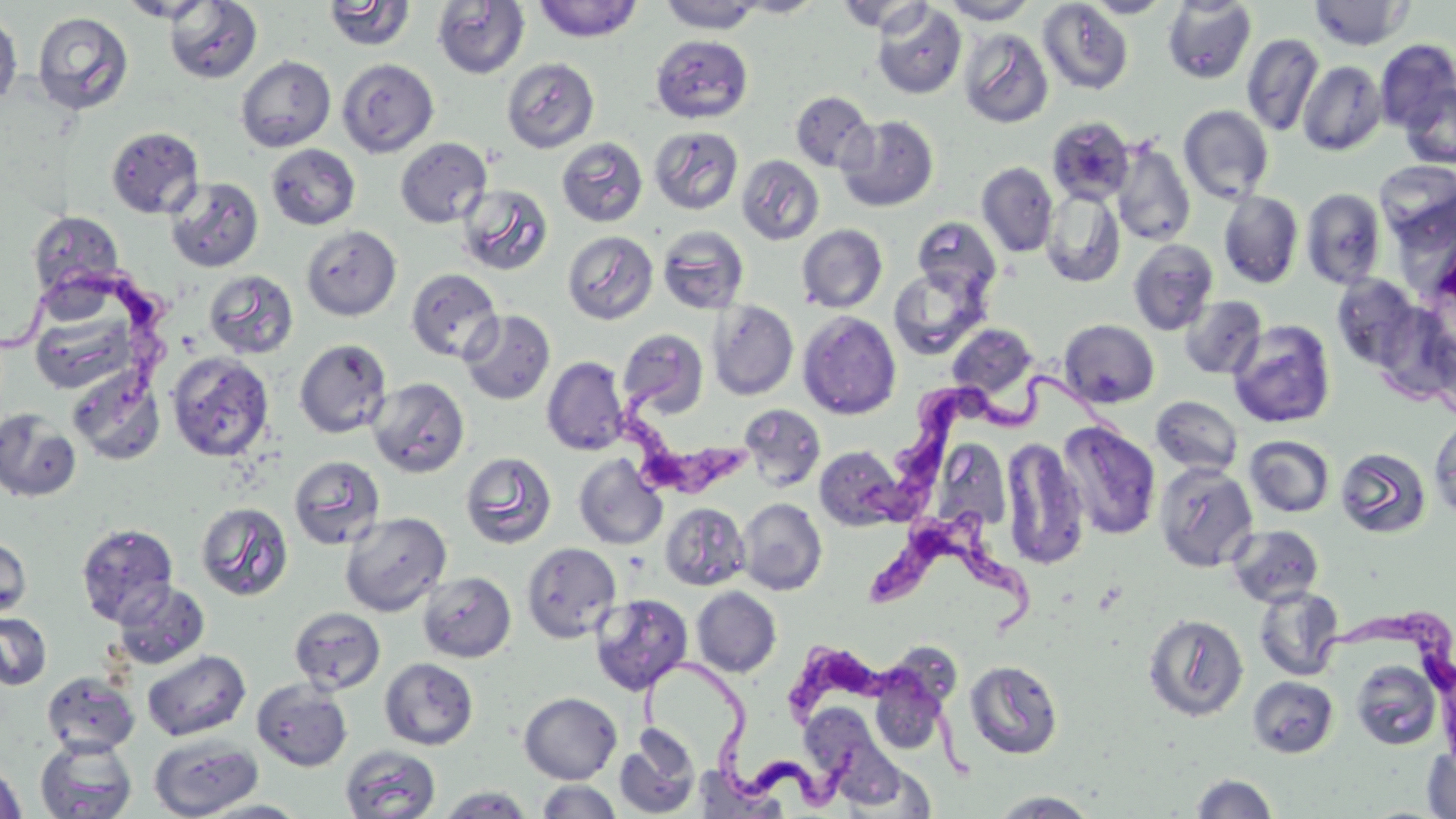

Approximate bounding boxes as [x1, y1, x2, y2] in pixels. Uninfected red blood cell locations: [116, 0, 218, 23], [532, 0, 644, 42], [734, 0, 825, 18], [940, 0, 1038, 24], [1083, 0, 1173, 18], [322, 1, 416, 52], [658, 1, 766, 33], [834, 1, 935, 34], [1037, 1, 1134, 95], [1162, 1, 1257, 84], [1309, 1, 1413, 50], [163, 2, 263, 83], [433, 2, 530, 78], [871, 3, 967, 99], [0, 9, 22, 110], [32, 11, 134, 115], [959, 28, 1053, 129], [651, 34, 753, 123], [1242, 34, 1323, 136], [1375, 39, 1456, 132], [235, 55, 336, 153], [501, 57, 599, 152], [338, 58, 439, 157], [1298, 60, 1387, 156], [1400, 81, 1456, 169], [790, 91, 876, 173], [1178, 105, 1274, 204], [837, 115, 939, 212], [1046, 116, 1135, 206], [106, 126, 204, 219], [649, 126, 743, 215], [395, 137, 492, 228], [556, 137, 649, 227], [1111, 141, 1195, 247], [266, 144, 361, 230], [736, 154, 825, 245], [976, 162, 1058, 257], [166, 177, 264, 272], [457, 184, 553, 276], [1041, 188, 1125, 287], [1301, 188, 1386, 289], [1218, 192, 1304, 288], [27, 211, 125, 303], [912, 217, 1001, 303], [797, 224, 888, 313], [301, 225, 401, 321], [656, 225, 750, 314], [562, 231, 659, 325], [1127, 239, 1218, 335], [888, 264, 990, 361], [406, 268, 502, 363], [203, 270, 299, 359], [1331, 274, 1422, 371], [1180, 296, 1267, 380], [708, 300, 799, 401], [28, 302, 142, 397], [1373, 305, 1456, 403], [459, 310, 556, 405], [798, 311, 901, 420], [1059, 319, 1159, 408], [1227, 319, 1336, 428], [947, 323, 1038, 402], [618, 328, 709, 419], [294, 338, 392, 439], [166, 352, 274, 462], [542, 356, 629, 455], [69, 370, 166, 465], [368, 378, 469, 478], [1151, 396, 1243, 476], [738, 404, 826, 491], [0, 408, 82, 502], [1429, 415, 1456, 521], [1058, 420, 1161, 541], [1244, 435, 1336, 518], [1000, 437, 1090, 570], [814, 446, 903, 530], [1335, 446, 1432, 540], [460, 451, 558, 550], [573, 454, 668, 550], [289, 455, 386, 549], [1154, 462, 1259, 573], [737, 498, 827, 595], [195, 501, 293, 601], [660, 502, 750, 590], [339, 511, 452, 616], [76, 523, 179, 626], [1226, 524, 1325, 607], [0, 535, 32, 621], [521, 542, 621, 643], [417, 571, 517, 663], [112, 581, 210, 670], [1252, 585, 1345, 682], [692, 586, 782, 677], [590, 593, 693, 695], [290, 606, 386, 695], [0, 611, 53, 691], [1142, 613, 1249, 723], [875, 641, 962, 726], [142, 650, 251, 741], [380, 657, 479, 750], [965, 660, 1063, 760], [1350, 660, 1441, 750], [870, 668, 949, 754], [41, 672, 141, 757], [1247, 676, 1338, 758], [252, 679, 352, 771], [519, 692, 622, 784], [614, 727, 701, 818], [149, 734, 262, 818], [35, 737, 137, 819], [340, 746, 441, 819], [1422, 746, 1456, 818], [0, 760, 28, 819], [1190, 773, 1279, 818], [537, 780, 622, 819], [436, 785, 535, 818], [990, 790, 1100, 818], [197, 799, 311, 818]. Trypanosoma brucei locations: [0, 262, 180, 399], [611, 353, 759, 510], [890, 368, 1145, 521], [863, 509, 1051, 651], [1311, 605, 1456, 750], [779, 621, 979, 789], [645, 652, 877, 810]. Slide-level diagnosis: Trypanosoma brucei. May-Grünwald-Giemsa-stained preparation. Light microscopy. Image is 1456×819 pixels. Single field of view. 1000x magnification. Thin blood smear.